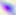

Summary:
  - Modality: photomicrograph
  - Identification: Toxoplasma gondii
  - Magnification: 400x